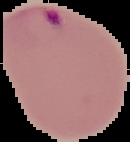

Summary:
  - Preparation: thin blood film
  - Image size: 130×142 pixels
  - Result: Plasmodium parasites identified
  - Image type: segmented cell region with the area outside set to black